Locate every uninfected red blood cell.
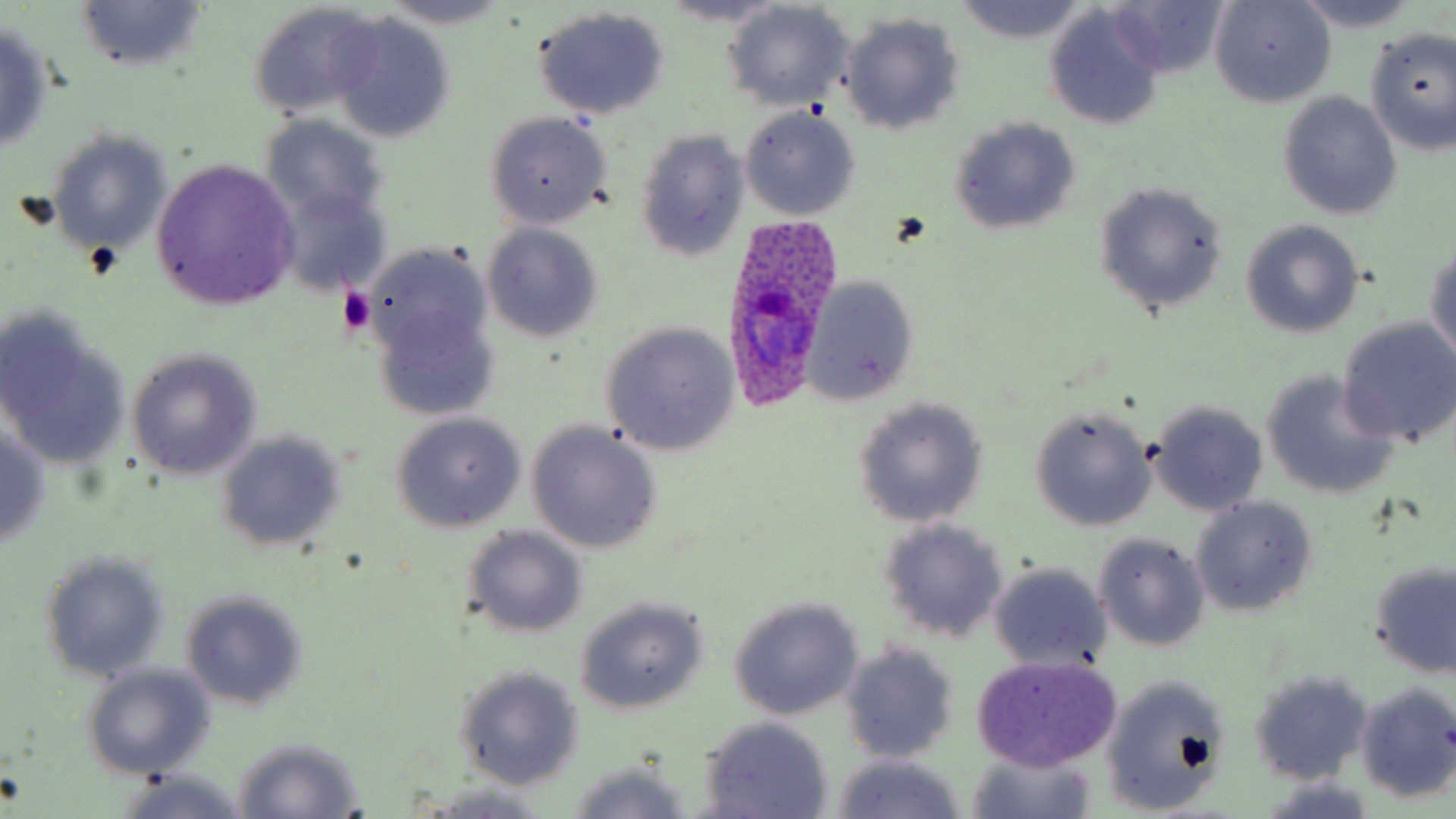
Approximate bounding boxes as (x1,y1)-(x2,y2) corner pairs in pixels.
Uninfected red blood cells: (1102,0)-(1230,80), (1211,0)-(1333,107), (1290,0)-(1425,32), (378,1)-(518,31), (953,1)-(1084,42), (74,2)-(207,72), (659,2)-(789,28), (721,3)-(855,111), (248,4)-(383,123), (533,7)-(671,120), (1043,8)-(1166,130), (840,12)-(965,135), (326,13)-(457,143), (0,20)-(56,153), (1363,28)-(1456,153), (1277,92)-(1402,221), (739,107)-(860,220), (484,111)-(612,230), (261,116)-(390,226), (947,117)-(1081,237), (634,127)-(748,262), (48,132)-(173,257), (151,160)-(300,309), (1093,181)-(1228,318), (272,184)-(391,296), (1242,219)-(1365,338), (482,223)-(604,344), (1426,242)-(1456,365), (365,258)-(501,419), (801,275)-(920,405), (0,315)-(130,474), (1337,319)-(1456,447), (600,323)-(739,456), (127,348)-(262,480), (1260,370)-(1399,500), (852,397)-(989,527), (1148,400)-(1269,516), (1030,407)-(1156,531), (390,413)-(526,532), (526,420)-(663,554), (0,422)-(53,551), (215,431)-(344,552), (1190,496)-(1319,616), (876,518)-(1009,644), (461,526)-(588,639), (1093,533)-(1211,651), (38,549)-(171,684), (1368,560)-(1456,678), (987,562)-(1113,676), (179,588)-(311,712), (575,598)-(709,714), (728,598)-(864,721), (840,641)-(961,762), (971,656)-(1123,770), (80,663)-(215,779), (453,665)-(583,791), (1247,667)-(1372,786), (1101,672)-(1231,816), (1354,681)-(1456,803), (698,716)-(834,818), (232,736)-(363,818), (967,747)-(1097,819), (828,754)-(969,819), (566,764)-(694,819), (115,770)-(251,819), (1257,777)-(1380,818), (419,782)-(552,815).

Platelet locations: (337,287)-(375,335). Plasmodium ovale-infected red blood cell locations: (724,214)-(838,410). Slide-level diagnosis: Plasmodium ovale. Thin blood smear. May-Grünwald-Giemsa-stained preparation. Captured at 1000x magnification. Image is 1456×819 pixels. Light microscopy. Single field of view.